Classify this cell by malaria status.
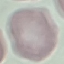
It is uninfected.

Cell patch, automatically extracted from a larger field of view and resized to 64 × 64 pixels. Giemsa stain. Thin blood smear. Photographed with a smartphone camera at the microscope eyepiece.